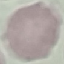

Result: no malaria parasites seen. Automatically extracted cell patch, resized to 64 × 64 pixels. Giemsa-stained preparation. Acquired by smartphone through the microscope eyepiece. Thin blood smear.